Report the malaria status of this cell.
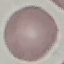
Uninfected.

Summary:
  - Stain: Giemsa
  - Preparation: thin blood smear
  - Capture: smartphone through the microscope eyepiece
  - Image type: automatically extracted cell patch, resized to 64 × 64 pixels